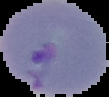

image type = segmented cell region on a black background
result = Plasmodium parasites detected
preparation = thin blood smear
image size = 109×97 pixels